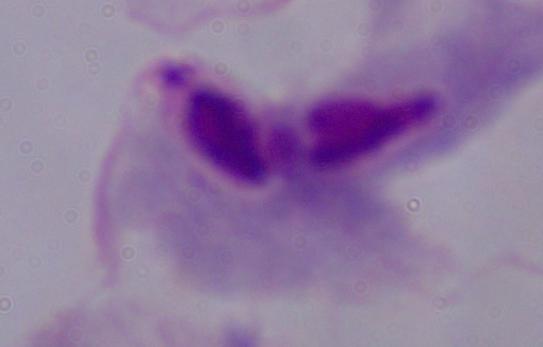
Summary:
  - Magnification: 1000x
  - Identification: trichomonad
  - Modality: micrograph